State which parasite is depicted.
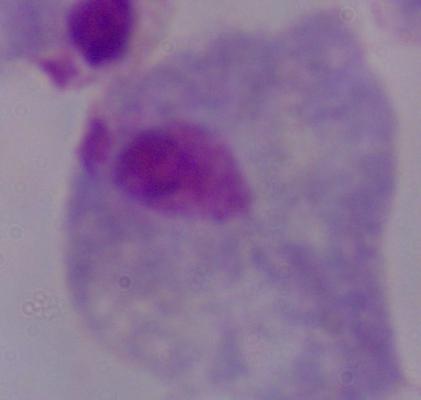

This is a trichomonad.

Summary:
  - Modality: micrograph
  - Magnification: 1000x